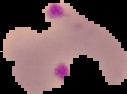

preparation = thin blood film
result = malaria parasites identified
image size = 127×94 pixels
image type = cell region segmented out of the field of view; surrounding area masked to black